Name the parasite shown.
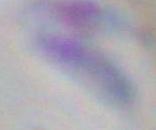

Toxoplasma gondii.

{
  "modality": "photomicrograph",
  "magnification": "1000x"
}